Outline each blood parasite and name the species.
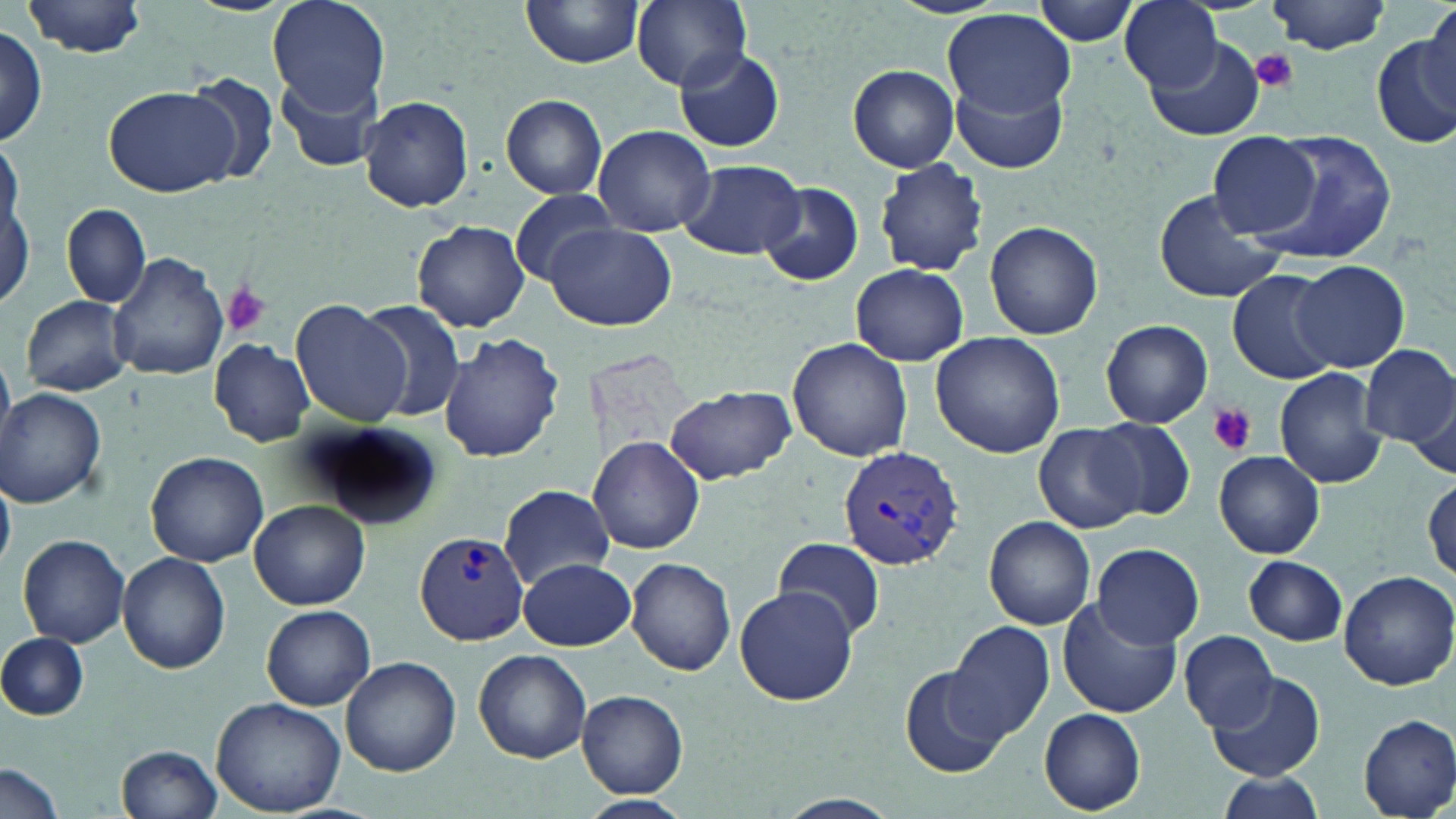
Approximate bounding boxes as [x1, y1, x2, y2] in pixels.
Plasmodium vivax-infected red blood cells: [837, 445, 964, 571], [412, 530, 528, 645].
No Plasmodium falciparum, Plasmodium ovale, Plasmodium malariae, Babesia divergens, or Trypanosoma brucei observed.

Uninfected red blood cell locations: [267, 0, 390, 115], [519, 0, 644, 70], [629, 0, 756, 92], [1031, 0, 1141, 45], [1120, 0, 1225, 94], [1269, 1, 1392, 53], [22, 2, 152, 58], [1424, 4, 1456, 98], [943, 10, 1079, 122], [1, 27, 48, 150], [1372, 32, 1456, 151], [1147, 36, 1265, 140], [674, 46, 786, 153], [847, 64, 959, 172], [184, 74, 281, 184], [277, 74, 387, 173], [952, 78, 1067, 176], [105, 85, 236, 196], [500, 94, 607, 200], [359, 98, 474, 211], [590, 125, 716, 238], [1251, 131, 1396, 261], [1209, 132, 1318, 238], [0, 137, 22, 251], [875, 157, 988, 278], [680, 158, 805, 260], [756, 180, 864, 287], [2, 185, 34, 310], [1152, 189, 1284, 304], [506, 190, 626, 284], [61, 204, 151, 308], [412, 220, 531, 332], [985, 220, 1104, 339], [545, 222, 675, 330], [109, 252, 229, 381], [1291, 259, 1411, 372], [850, 263, 969, 366], [1230, 269, 1343, 383], [20, 295, 133, 396], [290, 299, 412, 427], [357, 299, 470, 423], [1100, 320, 1212, 428], [929, 331, 1065, 458], [439, 332, 564, 463], [786, 337, 913, 462], [208, 339, 314, 446], [1359, 344, 1455, 446], [1274, 368, 1389, 489], [664, 383, 796, 484], [1404, 387, 1455, 482], [1, 388, 106, 509], [1090, 418, 1195, 520], [302, 423, 443, 529], [1033, 424, 1144, 534], [588, 436, 706, 555], [1214, 451, 1324, 559], [148, 452, 266, 566], [0, 474, 17, 569], [1423, 478, 1455, 582], [497, 484, 616, 590], [250, 501, 370, 609], [984, 515, 1096, 630], [15, 533, 132, 648], [773, 536, 884, 639], [1093, 545, 1204, 648], [117, 552, 230, 676], [1243, 555, 1348, 645], [519, 557, 636, 649], [626, 557, 734, 676], [1337, 570, 1456, 690], [734, 585, 856, 705], [1057, 599, 1181, 718], [262, 605, 375, 710], [946, 621, 1054, 742], [1179, 630, 1279, 731], [1, 633, 89, 719], [474, 649, 592, 763], [341, 656, 461, 775], [901, 665, 1007, 778], [1208, 672, 1324, 781], [576, 689, 689, 797], [211, 698, 347, 818], [1040, 708, 1145, 815], [1358, 714, 1456, 818], [118, 744, 221, 819], [0, 762, 66, 819], [1211, 774, 1322, 818], [767, 793, 905, 819], [576, 794, 692, 819]. Platelet locations: [1251, 49, 1297, 92], [219, 282, 272, 337], [1206, 402, 1258, 456]. Slide-level diagnosis: Plasmodium vivax. Single field of view. Thin blood smear. Light microscopy. May-Grünwald-Giemsa-stained preparation. Captured at 1000x magnification. Image is 1456×819 pixels.